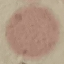
malaria_status: uninfected
image_type: cell patch, automatically extracted from a larger field of view and resized to 64 × 64 pixels
stain: Giemsa
capture: smartphone through the microscope eyepiece
preparation: thin blood film